Assess this cell for malaria.
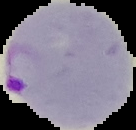

Parasitized.

Cell region segmented out of the field of view; the surrounding area is masked to black. Image is 136×130 pixels. From a thin blood smear.